Give the position of every malaria parasite and every leukocyte.
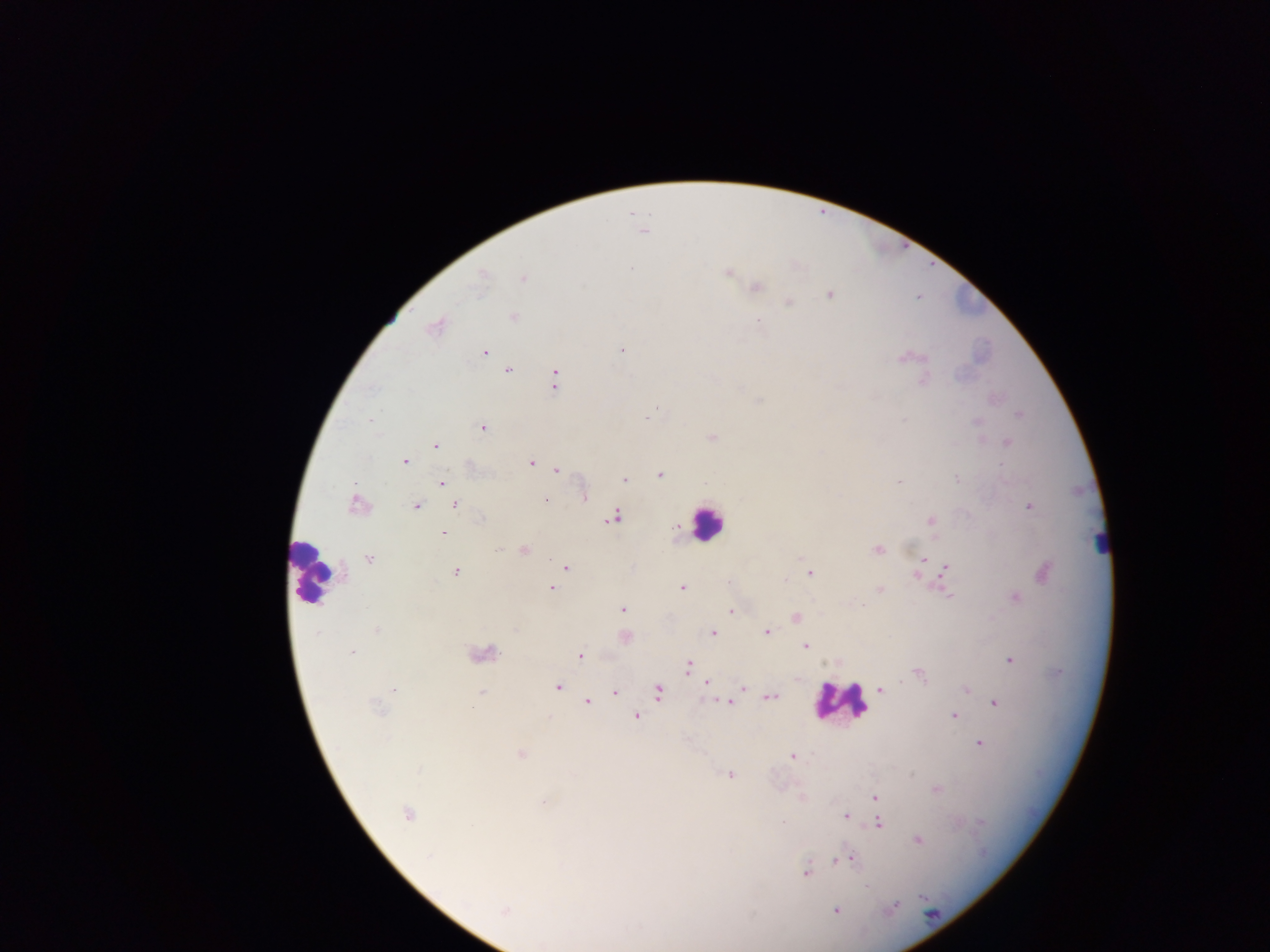

Approximate centers as [x, y] in pixels.
Malaria parasites: [643, 231], [631, 269], [728, 273], [482, 276], [523, 278], [757, 287], [829, 295], [789, 302], [512, 317], [759, 322], [436, 327], [621, 350], [484, 352], [904, 358], [509, 371], [554, 380], [923, 381], [655, 410], [651, 414], [1018, 415], [370, 420], [977, 422], [482, 428], [712, 438], [1007, 442], [436, 446], [405, 462], [531, 463], [1001, 464], [556, 469], [660, 475], [957, 478], [625, 480], [899, 481], [442, 483], [585, 497], [545, 500], [356, 504], [455, 505], [415, 507], [1029, 507], [613, 517], [481, 518], [931, 521], [443, 532], [499, 548], [877, 549], [524, 550], [368, 559], [925, 559], [566, 567], [947, 569], [456, 572], [1044, 572], [809, 574], [916, 575], [785, 579], [682, 587], [552, 588], [879, 589], [947, 594], [1016, 597], [622, 609], [731, 610], [795, 618], [376, 631], [767, 632], [713, 633], [625, 637], [806, 646], [351, 652], [484, 655], [580, 656], [1011, 660], [689, 667], [919, 675], [707, 683], [558, 687], [742, 688], [881, 689], [394, 690], [966, 690], [615, 691], [481, 692], [659, 692], [771, 697], [587, 702], [729, 703], [995, 703], [378, 707], [637, 716], [954, 716], [980, 744], [521, 754], [792, 756], [419, 770], [730, 775], [937, 790], [875, 798], [543, 802], [408, 814], [846, 816], [783, 822], [880, 823], [918, 840], [429, 857], [851, 859], [837, 860], [805, 872], [866, 886], [894, 906], [505, 910], [836, 911].
Leukocytes: [706, 522], [1101, 546], [312, 571], [840, 701].

preparation = thick blood smear
field of view = single
image size = 1270×952 pixels
country = Ghana
capture = mobile-phone photograph through a microscope